Identify the parasite.
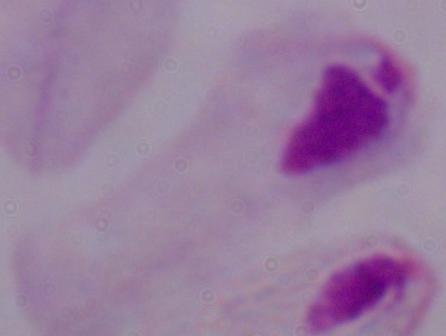

A trichomonad.

1000x magnification. Photomicrograph.